Assess this cell for malaria.
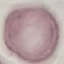
It is uninfected.

Cell patch, automatically extracted from a larger field of view and resized to 64 × 64 pixels. Thin blood film. Giemsa stain. Photographed with a smartphone camera at the microscope eyepiece.